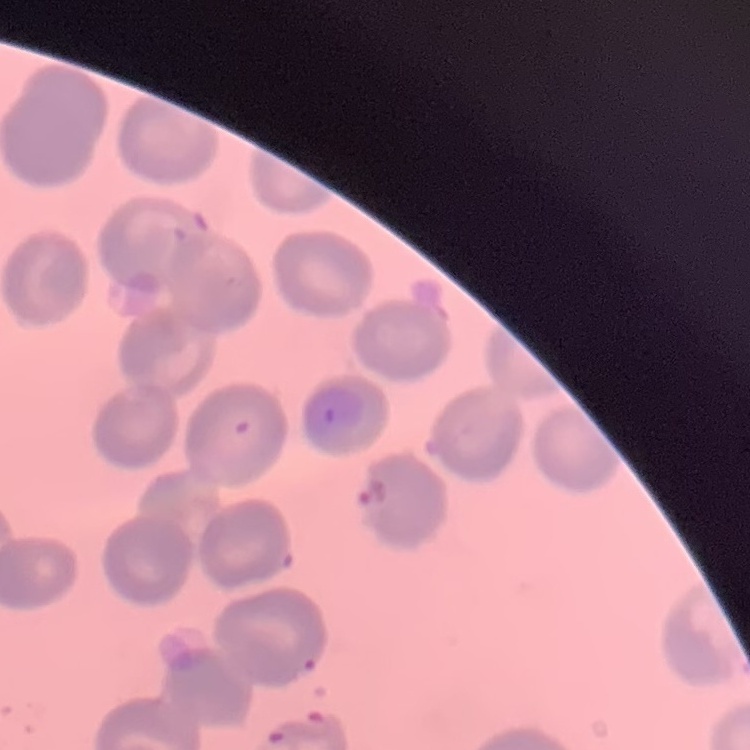
The red blood cells show no rouleaux formation. Thin blood film. Field's or Giemsa stain. Square crop of a larger photomicrograph.